Outline each blood parasite and name the species.
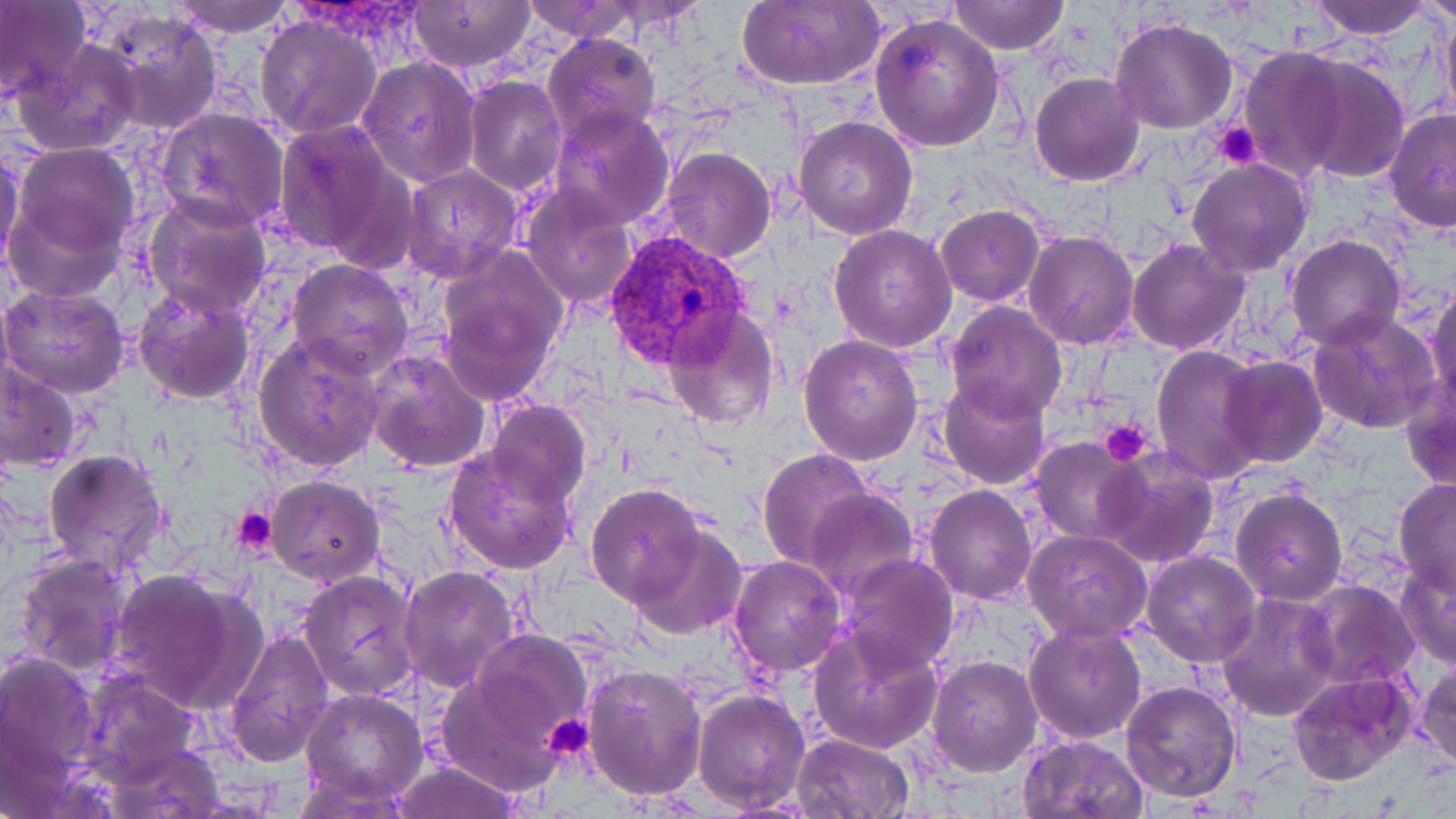

Approximate bounding boxes as named x1/y1/x2/y2 corners in pixels.
Plasmodium vivax-infected red blood cells: (x1=605, y1=229, x2=747, y2=370).
No Plasmodium falciparum, Plasmodium ovale, Plasmodium malariae, Babesia divergens, or Trypanosoma brucei observed.

Uninfected red blood cell locations: (x1=0, y1=0, x2=89, y2=102), (x1=170, y1=0, x2=296, y2=38), (x1=406, y1=0, x2=535, y2=70), (x1=520, y1=0, x2=640, y2=43), (x1=736, y1=0, x2=885, y2=91), (x1=950, y1=0, x2=1068, y2=54), (x1=1303, y1=0, x2=1437, y2=39), (x1=1418, y1=0, x2=1456, y2=27), (x1=1436, y1=3, x2=1456, y2=131), (x1=100, y1=10, x2=221, y2=134), (x1=869, y1=10, x2=1005, y2=153), (x1=256, y1=15, x2=381, y2=139), (x1=1111, y1=17, x2=1238, y2=133), (x1=542, y1=33, x2=662, y2=146), (x1=13, y1=37, x2=143, y2=156), (x1=1236, y1=47, x2=1353, y2=182), (x1=463, y1=48, x2=654, y2=164), (x1=1293, y1=53, x2=1411, y2=184), (x1=358, y1=56, x2=481, y2=186), (x1=1030, y1=73, x2=1144, y2=186), (x1=464, y1=74, x2=566, y2=194), (x1=549, y1=104, x2=675, y2=227), (x1=1383, y1=107, x2=1456, y2=232), (x1=155, y1=108, x2=291, y2=232), (x1=793, y1=115, x2=919, y2=240), (x1=273, y1=119, x2=413, y2=263), (x1=8, y1=143, x2=142, y2=269), (x1=0, y1=144, x2=25, y2=274), (x1=657, y1=147, x2=775, y2=263), (x1=1186, y1=158, x2=1313, y2=277), (x1=401, y1=164, x2=523, y2=283), (x1=520, y1=186, x2=638, y2=309), (x1=5, y1=193, x2=124, y2=303), (x1=144, y1=194, x2=273, y2=319), (x1=935, y1=205, x2=1045, y2=307), (x1=829, y1=223, x2=958, y2=353), (x1=1023, y1=228, x2=1139, y2=349), (x1=1286, y1=236, x2=1405, y2=352), (x1=1129, y1=239, x2=1248, y2=354), (x1=436, y1=252, x2=567, y2=401), (x1=287, y1=259, x2=414, y2=377), (x1=0, y1=284, x2=130, y2=400), (x1=1426, y1=284, x2=1456, y2=414), (x1=131, y1=288, x2=256, y2=405), (x1=944, y1=301, x2=1068, y2=421), (x1=663, y1=308, x2=780, y2=430), (x1=1306, y1=309, x2=1443, y2=436), (x1=253, y1=331, x2=386, y2=472), (x1=799, y1=333, x2=925, y2=466), (x1=1151, y1=346, x2=1271, y2=484), (x1=365, y1=349, x2=492, y2=474), (x1=1217, y1=356, x2=1328, y2=468), (x1=1, y1=358, x2=85, y2=476), (x1=938, y1=377, x2=1050, y2=489), (x1=1401, y1=380, x2=1456, y2=495), (x1=485, y1=400, x2=591, y2=506), (x1=1030, y1=438, x2=1145, y2=545), (x1=444, y1=445, x2=579, y2=575), (x1=42, y1=447, x2=169, y2=576), (x1=758, y1=449, x2=874, y2=569), (x1=1096, y1=449, x2=1220, y2=568), (x1=264, y1=475, x2=384, y2=587), (x1=1393, y1=479, x2=1456, y2=597), (x1=586, y1=483, x2=705, y2=606), (x1=925, y1=484, x2=1037, y2=603), (x1=1230, y1=488, x2=1346, y2=606), (x1=806, y1=489, x2=920, y2=599), (x1=628, y1=526, x2=746, y2=640), (x1=1022, y1=530, x2=1150, y2=642), (x1=1141, y1=551, x2=1261, y2=668), (x1=13, y1=553, x2=133, y2=676), (x1=840, y1=553, x2=959, y2=675), (x1=729, y1=554, x2=847, y2=676), (x1=1396, y1=560, x2=1456, y2=670), (x1=398, y1=566, x2=520, y2=691), (x1=107, y1=568, x2=261, y2=715), (x1=298, y1=570, x2=421, y2=702), (x1=1301, y1=580, x2=1419, y2=689), (x1=1216, y1=591, x2=1342, y2=721), (x1=1024, y1=621, x2=1147, y2=742), (x1=809, y1=627, x2=943, y2=753), (x1=223, y1=628, x2=334, y2=766), (x1=469, y1=630, x2=594, y2=744), (x1=0, y1=647, x2=102, y2=800), (x1=926, y1=655, x2=1043, y2=776), (x1=436, y1=660, x2=576, y2=790), (x1=1415, y1=661, x2=1456, y2=773), (x1=582, y1=664, x2=708, y2=799), (x1=73, y1=670, x2=204, y2=789), (x1=1288, y1=672, x2=1419, y2=788), (x1=1119, y1=680, x2=1243, y2=803), (x1=694, y1=687, x2=810, y2=814), (x1=301, y1=689, x2=427, y2=806), (x1=793, y1=732, x2=914, y2=817), (x1=1018, y1=734, x2=1149, y2=819), (x1=103, y1=737, x2=229, y2=817), (x1=388, y1=761, x2=522, y2=819). Platelet locations: (x1=1213, y1=123, x2=1264, y2=169), (x1=1099, y1=418, x2=1153, y2=466), (x1=233, y1=508, x2=279, y2=559), (x1=543, y1=712, x2=593, y2=763). Slide-level diagnosis: Plasmodium vivax. 1000x magnification. Thin blood smear. May-Grünwald-Giemsa-stained preparation. Image is 1456×819 pixels. Single field of view. Optical microscopy.